Locate every uninfected red blood cell.
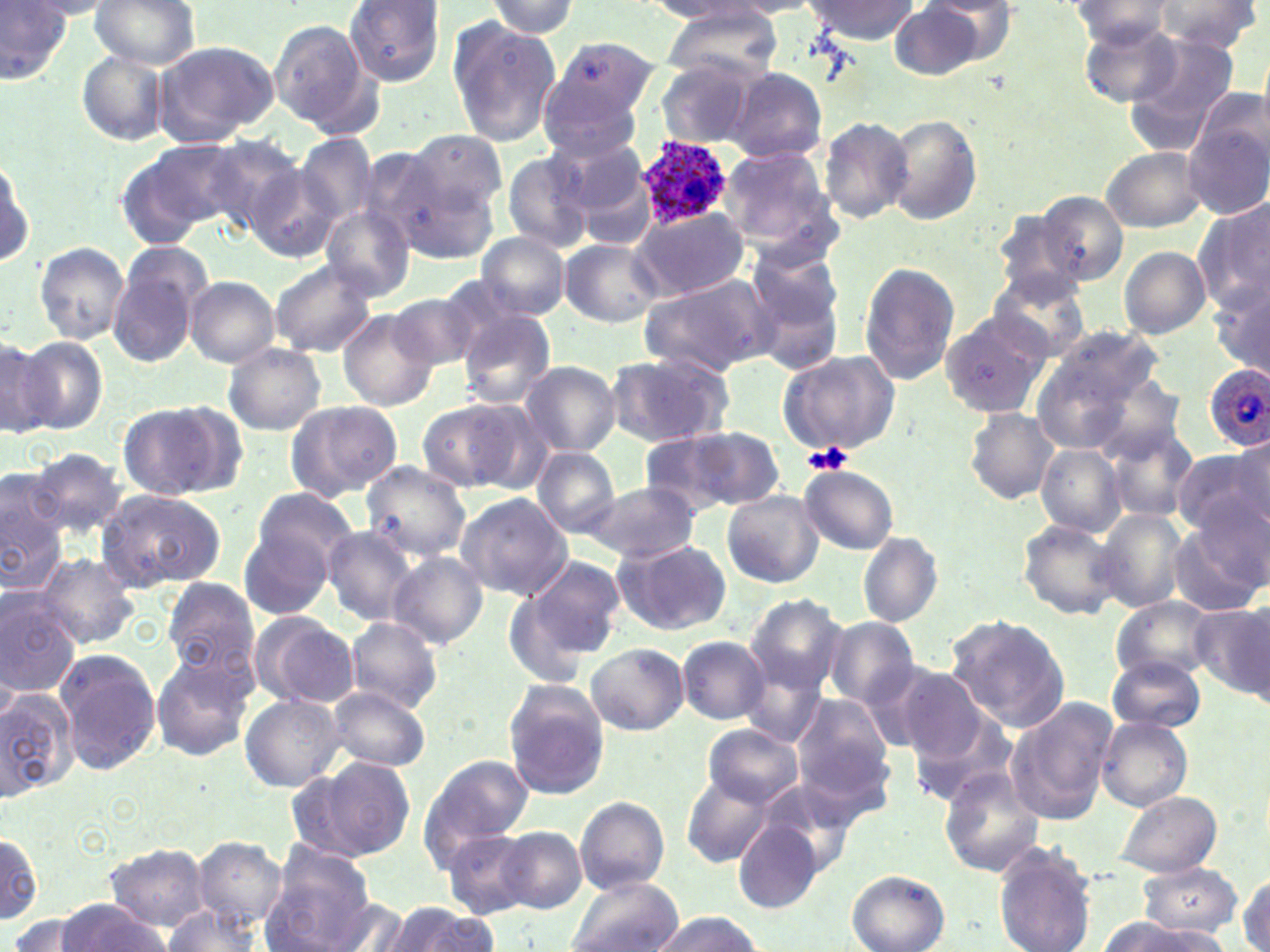
Approximate bounding boxes as (x1, y1, x2, y2) in pixels.
Uninfected red blood cells: (89, 0, 201, 70), (806, 0, 920, 44), (0, 1, 75, 88), (484, 1, 579, 37), (642, 1, 762, 23), (926, 1, 1019, 65), (1155, 1, 1262, 52), (344, 2, 446, 85), (889, 2, 992, 80), (1067, 3, 1180, 48), (661, 5, 784, 79), (445, 17, 560, 148), (268, 18, 376, 132), (1079, 19, 1186, 107), (1123, 34, 1241, 149), (546, 36, 659, 132), (153, 41, 276, 148), (77, 51, 169, 145), (660, 61, 757, 145), (727, 68, 826, 161), (542, 73, 647, 163), (1183, 106, 1270, 222), (885, 114, 982, 226), (820, 115, 915, 224), (406, 129, 508, 216), (293, 134, 378, 226), (195, 136, 304, 233), (553, 136, 647, 219), (122, 139, 244, 244), (354, 146, 452, 253), (719, 147, 833, 249), (1100, 147, 1207, 232), (500, 150, 598, 253), (0, 152, 34, 274), (245, 166, 344, 264), (403, 185, 499, 264), (1038, 190, 1131, 286), (1193, 197, 1270, 324), (321, 206, 415, 301), (630, 208, 750, 302), (991, 212, 1086, 304), (476, 231, 571, 320), (118, 239, 214, 321), (561, 240, 663, 327), (34, 242, 129, 344), (1120, 247, 1210, 338), (742, 248, 848, 377), (268, 260, 380, 359), (859, 262, 960, 385), (108, 264, 201, 369), (988, 273, 1090, 363), (637, 275, 773, 378), (185, 276, 280, 368), (1213, 276, 1270, 384), (389, 291, 486, 373), (939, 307, 1052, 416), (339, 310, 438, 411), (459, 311, 556, 408), (1032, 326, 1164, 452), (1, 337, 55, 437), (11, 337, 108, 436), (223, 342, 326, 436), (776, 349, 899, 458), (604, 351, 735, 449), (517, 360, 620, 457), (283, 399, 403, 502), (416, 400, 525, 492), (117, 401, 237, 501), (461, 403, 560, 496), (965, 409, 1058, 503), (1104, 422, 1200, 520), (655, 427, 783, 513), (1231, 437, 1269, 526), (1036, 443, 1127, 537), (1176, 444, 1269, 537), (531, 447, 619, 536), (28, 448, 127, 536), (360, 461, 472, 562), (800, 465, 899, 555), (0, 475, 68, 593), (582, 481, 701, 562), (252, 486, 358, 580), (95, 490, 225, 590), (723, 490, 822, 588), (455, 493, 573, 601), (1096, 508, 1189, 613), (1165, 514, 1269, 617), (1016, 518, 1123, 622), (323, 525, 422, 626), (239, 531, 332, 621), (857, 532, 942, 627), (614, 538, 731, 635), (389, 551, 488, 649), (31, 554, 137, 650), (518, 555, 625, 665), (162, 580, 259, 681), (0, 588, 80, 698), (744, 593, 850, 695), (1112, 598, 1216, 682), (1192, 604, 1270, 700), (250, 612, 359, 708), (945, 613, 1071, 732), (344, 617, 443, 715), (822, 619, 920, 709), (679, 636, 769, 723), (587, 642, 688, 736), (54, 647, 161, 776), (738, 650, 834, 749), (150, 651, 256, 762), (1107, 658, 1205, 733), (884, 665, 990, 759), (503, 683, 609, 799), (0, 686, 79, 799), (324, 686, 431, 772), (238, 694, 346, 793), (790, 694, 895, 799), (1007, 699, 1116, 823), (911, 709, 1019, 805), (1096, 716, 1193, 811), (704, 726, 802, 806), (301, 754, 418, 863), (421, 754, 534, 859), (938, 768, 1044, 878), (681, 772, 773, 866), (1114, 790, 1221, 877), (575, 796, 669, 894), (734, 821, 824, 911), (496, 826, 585, 914), (441, 827, 545, 920), (0, 829, 45, 927), (193, 837, 284, 925), (992, 842, 1097, 952), (104, 843, 210, 929), (261, 849, 379, 952), (1136, 863, 1243, 936), (846, 870, 950, 952), (1237, 874, 1269, 952), (565, 876, 682, 952), (321, 896, 417, 952), (53, 900, 171, 951), (381, 901, 494, 952), (159, 905, 266, 951), (8, 912, 99, 951), (647, 912, 765, 951), (1098, 919, 1223, 952).

Plasmodium ovale-infected red blood cell locations: (633, 136, 735, 227), (1204, 362, 1269, 449). Platelet locations: (803, 443, 853, 476). Slide-level diagnosis: Plasmodium ovale. Image is 1270×952 pixels. Light microscopy. One field of a larger specimen. Thin blood film. 1000x magnification. May-Grünwald-Giemsa stain.